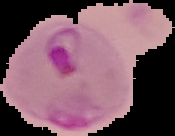

Summary:
  - Image type: segmented cell region with the area outside set to black
  - Preparation: thin blood film
  - Image size: 175×136 pixels
  - Malaria status: parasitized